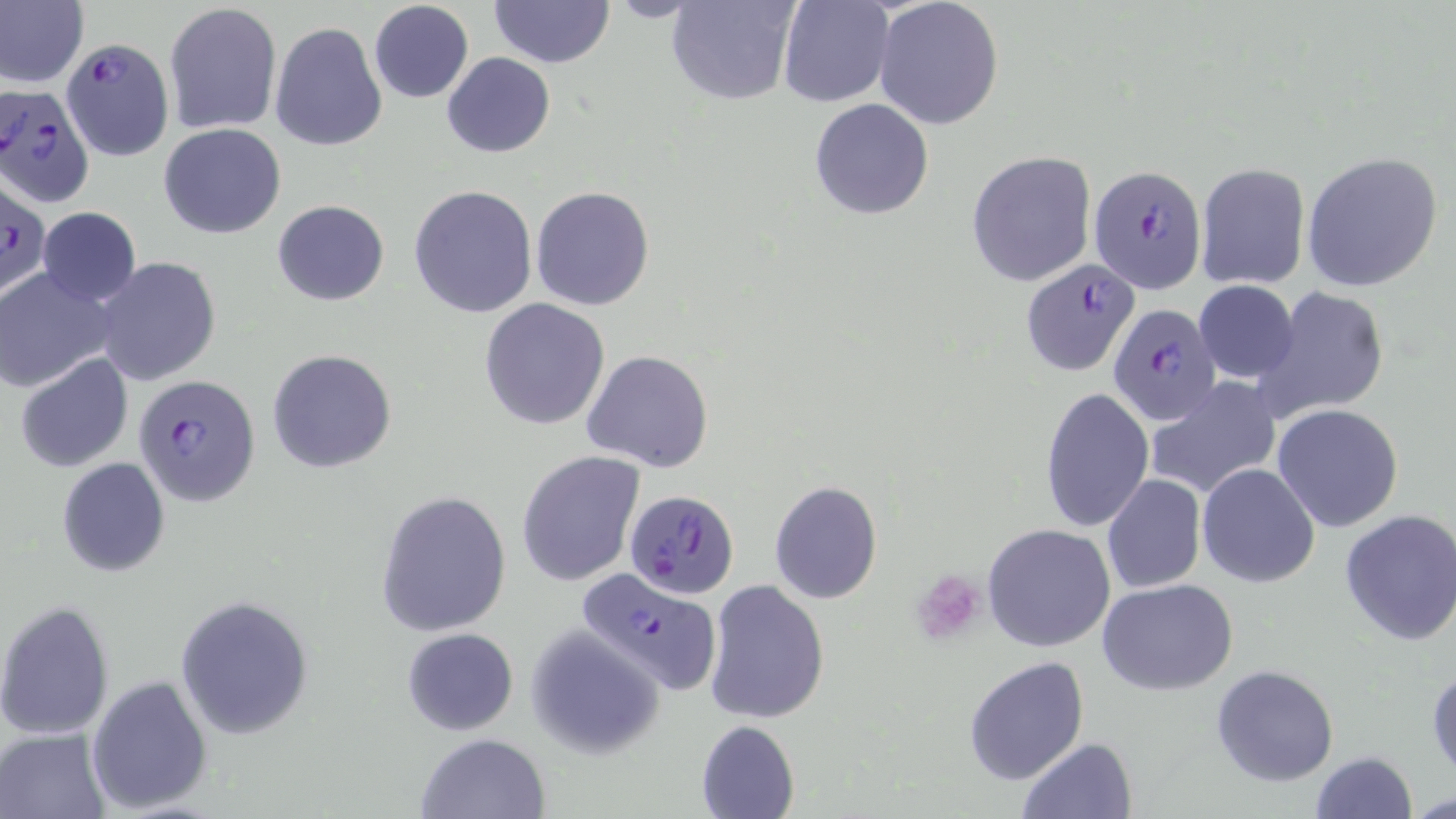

Approximate bounding boxes as (x1, y1, x2, y2) in pixels. Platelet locations: (909, 569, 987, 648). Plasmodium falciparum-infected red blood cell locations: (57, 36, 173, 164), (1, 86, 94, 208), (1090, 164, 1207, 291), (1, 179, 48, 301), (1019, 259, 1140, 376), (1107, 301, 1222, 427), (134, 375, 260, 505), (627, 491, 742, 602), (575, 565, 723, 695). Uninfected red blood cell locations: (0, 0, 87, 89), (489, 0, 615, 68), (666, 0, 800, 106), (777, 0, 892, 107), (874, 0, 1005, 130), (164, 2, 282, 135), (368, 2, 473, 104), (271, 21, 388, 151), (442, 52, 554, 158), (809, 98, 935, 220), (158, 122, 287, 239), (967, 150, 1096, 286), (1300, 151, 1444, 292), (1195, 163, 1310, 290), (409, 185, 538, 319), (530, 185, 655, 311), (272, 199, 389, 306), (36, 207, 142, 307), (94, 257, 219, 387), (0, 266, 114, 392), (1193, 279, 1300, 384), (1250, 286, 1389, 424), (479, 298, 610, 430), (267, 348, 397, 474), (582, 349, 715, 473), (14, 354, 133, 473), (1149, 377, 1281, 501), (1039, 387, 1154, 532), (1271, 404, 1404, 532), (516, 452, 645, 586), (57, 457, 170, 577), (1196, 463, 1321, 588), (1101, 475, 1206, 593), (769, 480, 882, 604), (376, 490, 511, 636), (1339, 509, 1456, 648), (982, 523, 1115, 652), (1098, 578, 1240, 695), (704, 580, 829, 726), (177, 597, 312, 738), (0, 601, 116, 741), (525, 627, 665, 757), (400, 628, 519, 735), (964, 656, 1088, 784), (1211, 664, 1339, 786), (1428, 665, 1455, 779), (86, 674, 214, 814), (696, 720, 799, 819), (0, 728, 109, 817), (414, 733, 551, 819), (1017, 738, 1136, 819), (1307, 751, 1417, 819), (1410, 792, 1456, 818). Slide-level diagnosis: Plasmodium falciparum. 1000x magnification. Light microscopy. Single field of view. Image is 1456×819 pixels. May-Grünwald-Giemsa-stained preparation. Thin blood film.